Locate every uninfected red blood cell.
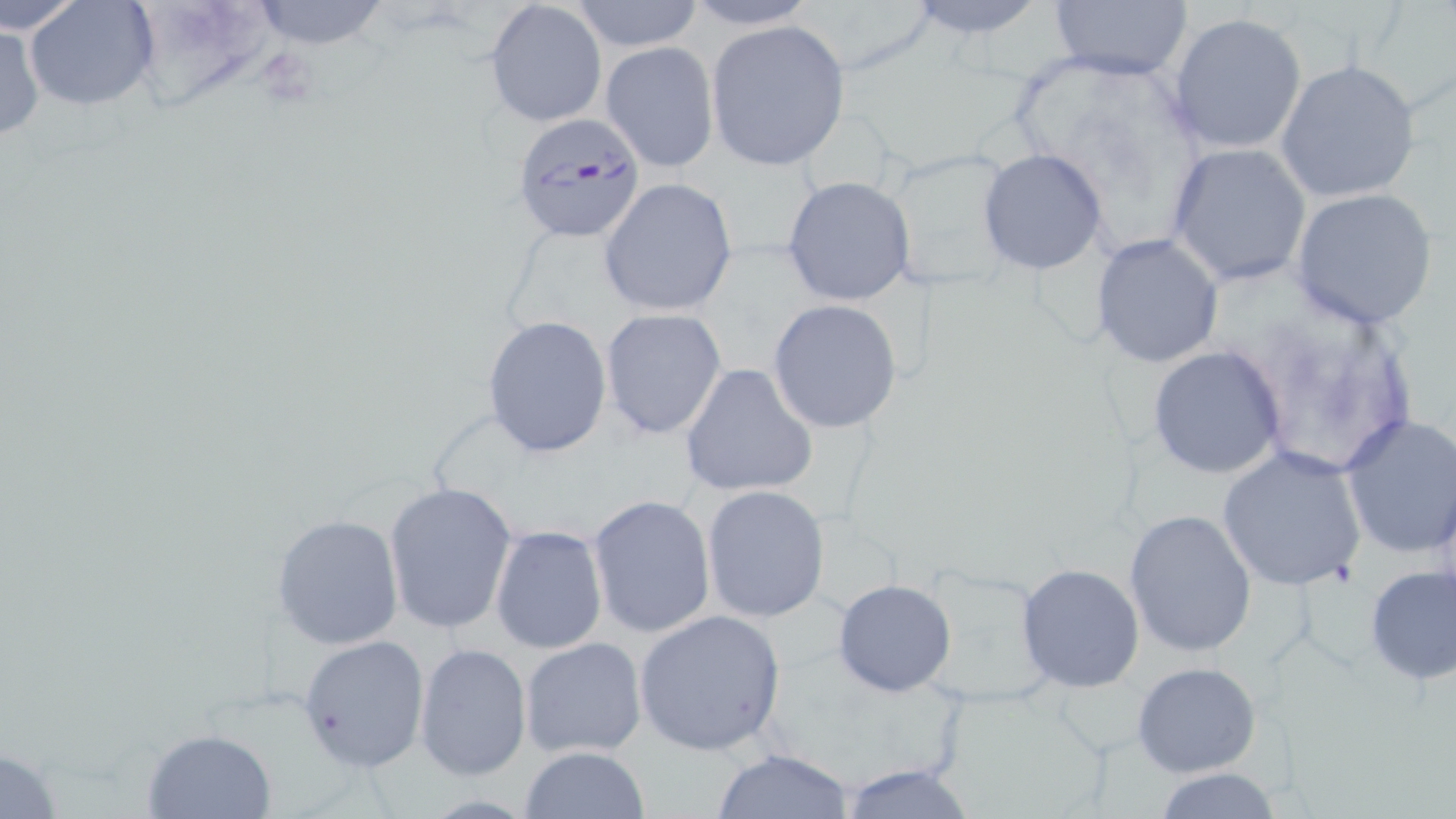

Approximate bounding boxes as (x1, y1, x2, y2) in pixels.
Uninfected red blood cells: (0, 0, 87, 38), (26, 0, 160, 111), (244, 0, 395, 51), (568, 0, 708, 52), (898, 0, 1054, 44), (1044, 0, 1194, 82), (486, 1, 607, 129), (677, 2, 825, 29), (1168, 12, 1307, 153), (704, 19, 850, 170), (0, 21, 46, 145), (601, 41, 720, 173), (1275, 59, 1423, 204), (1167, 144, 1313, 287), (976, 148, 1108, 276), (781, 175, 916, 306), (596, 178, 738, 316), (1291, 188, 1440, 330), (1089, 233, 1224, 368), (768, 300, 904, 434), (599, 308, 726, 439), (483, 314, 612, 457), (1148, 346, 1286, 480), (680, 363, 818, 499), (1340, 413, 1456, 559), (1216, 446, 1367, 592), (383, 481, 518, 636), (701, 485, 830, 624), (586, 495, 714, 638), (1124, 508, 1257, 658), (271, 515, 405, 650), (489, 524, 608, 653), (1015, 563, 1145, 692), (1362, 563, 1456, 686), (832, 578, 958, 698), (633, 610, 786, 756), (296, 634, 430, 773), (519, 636, 647, 759), (413, 642, 531, 781), (1131, 662, 1262, 777), (140, 727, 277, 817), (0, 742, 66, 819), (517, 746, 652, 819), (713, 747, 858, 819), (833, 766, 980, 819), (1150, 766, 1286, 819).

Plasmodium falciparum-infected red blood cell locations: (509, 115, 645, 243). Slide-level diagnosis: Plasmodium falciparum. Light microscopy. Thin blood smear. 1000x magnification. May-Grünwald-Giemsa stain. Image is 1456×819 pixels. One field of a larger specimen.